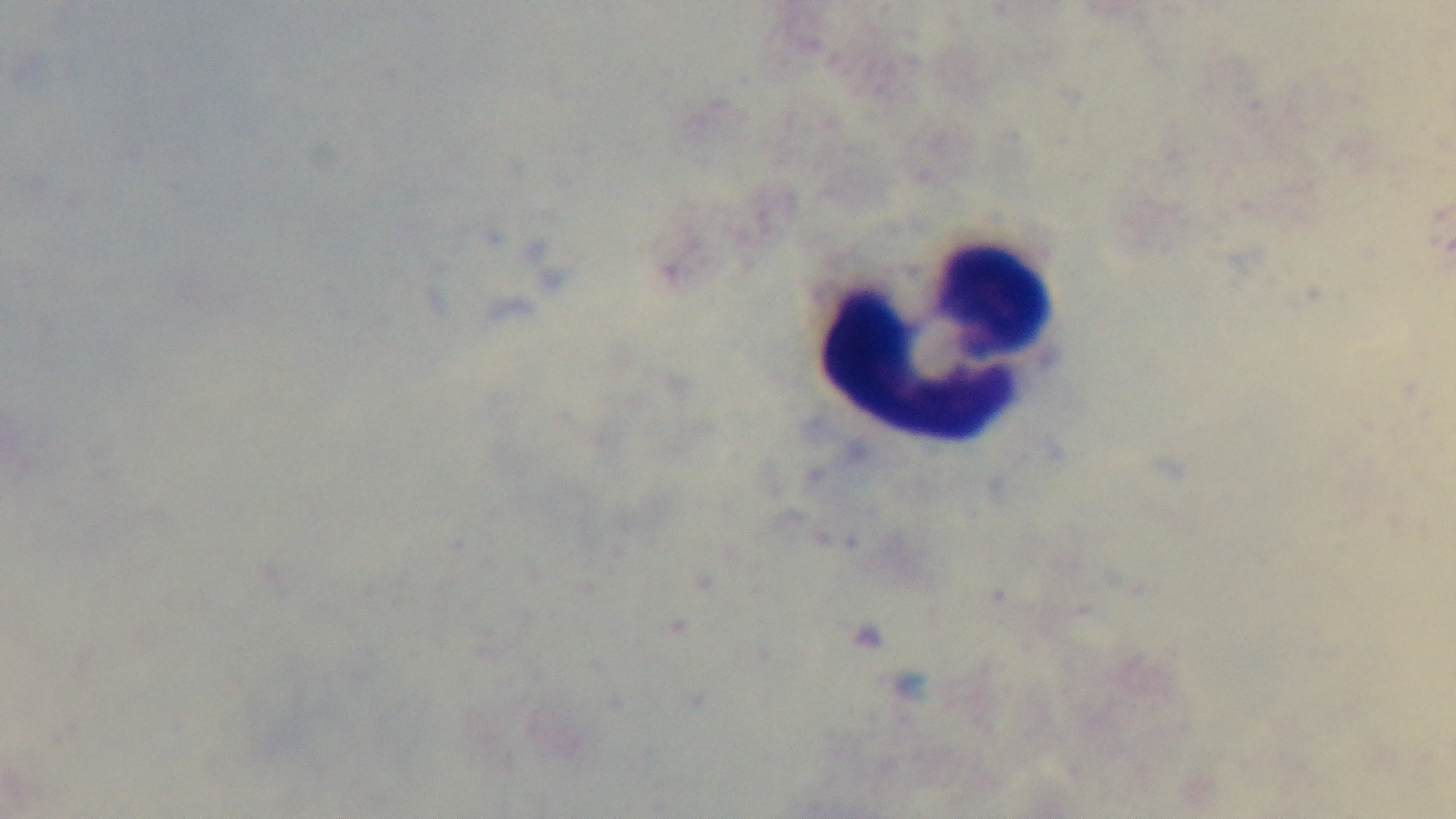

preparation: thick smear
malaria_status: negative
field_of_view: one from the slide
modality: light microscopy
objective: 100x oil immersion
capture: mounted 4K digital camera
stain: Giemsa